State the preparation type.
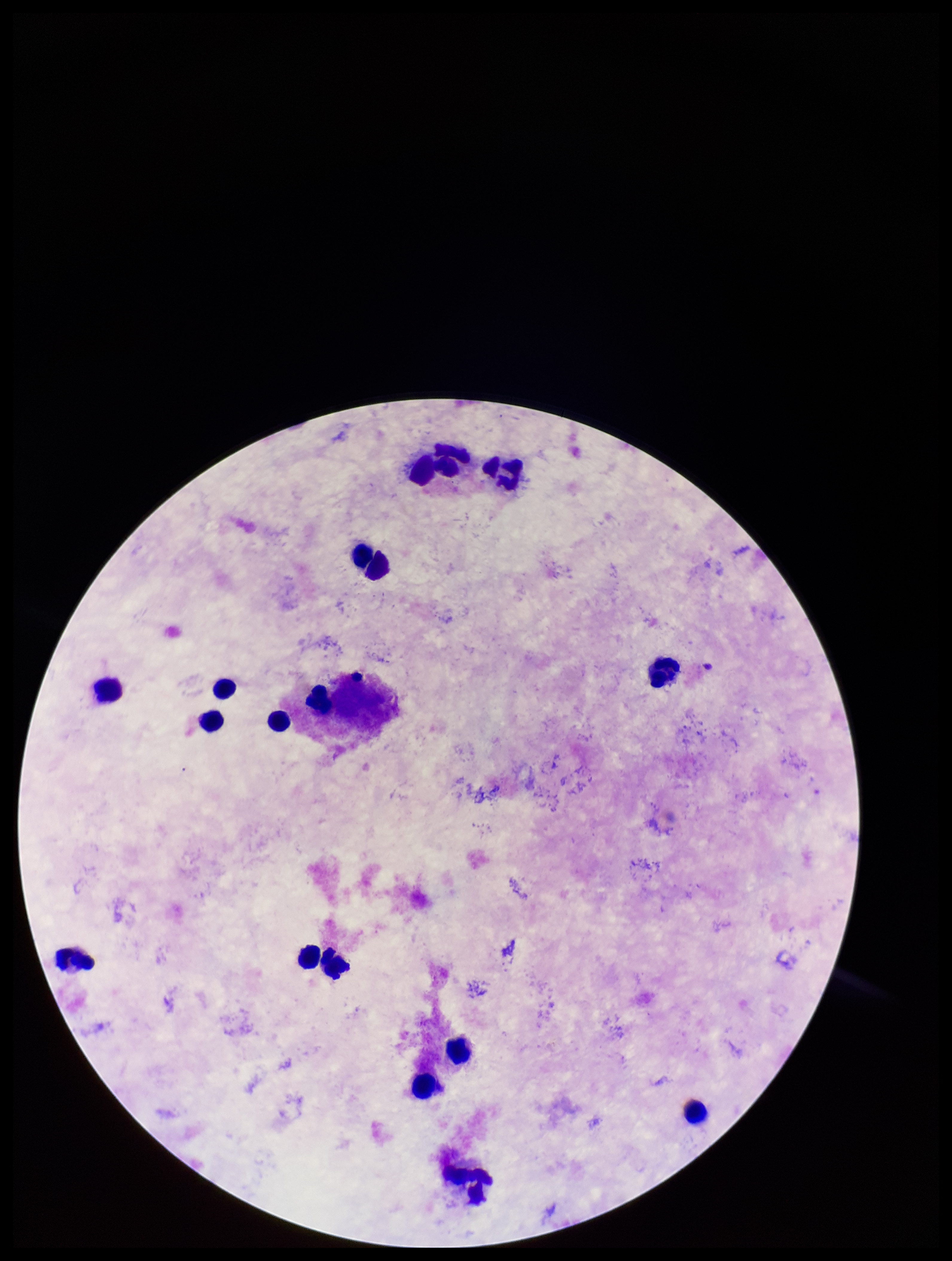
It is a thick blood smear.

leukocyte_count: 16
plasmodium_parasites: none seen
patient_malaria_status: negative
image_size: 952×1261 pixels
field_of_view: single
capture: smartphone photograph through the microscope eyepiece
parasite_count: 0
stain: Giemsa